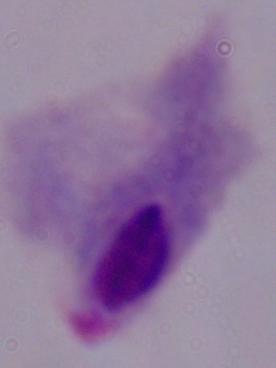
1000x magnification. A trichomonad is shown. Micrograph.